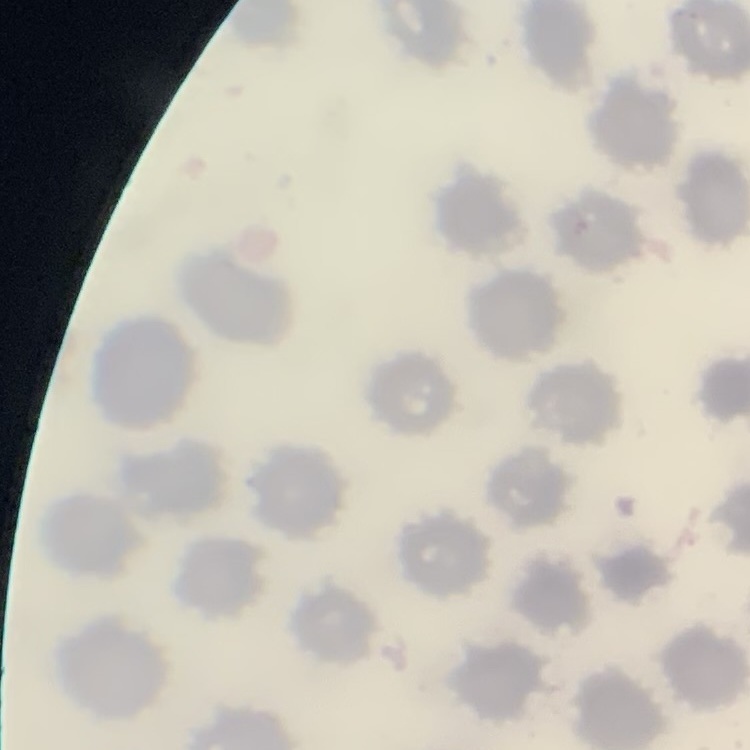
{
  "erythrocyte_morphology": "no rouleaux formation",
  "image_type": "one tile cut from a larger photomicrograph",
  "preparation": "thin blood smear",
  "stain": "Field's or Giemsa"
}